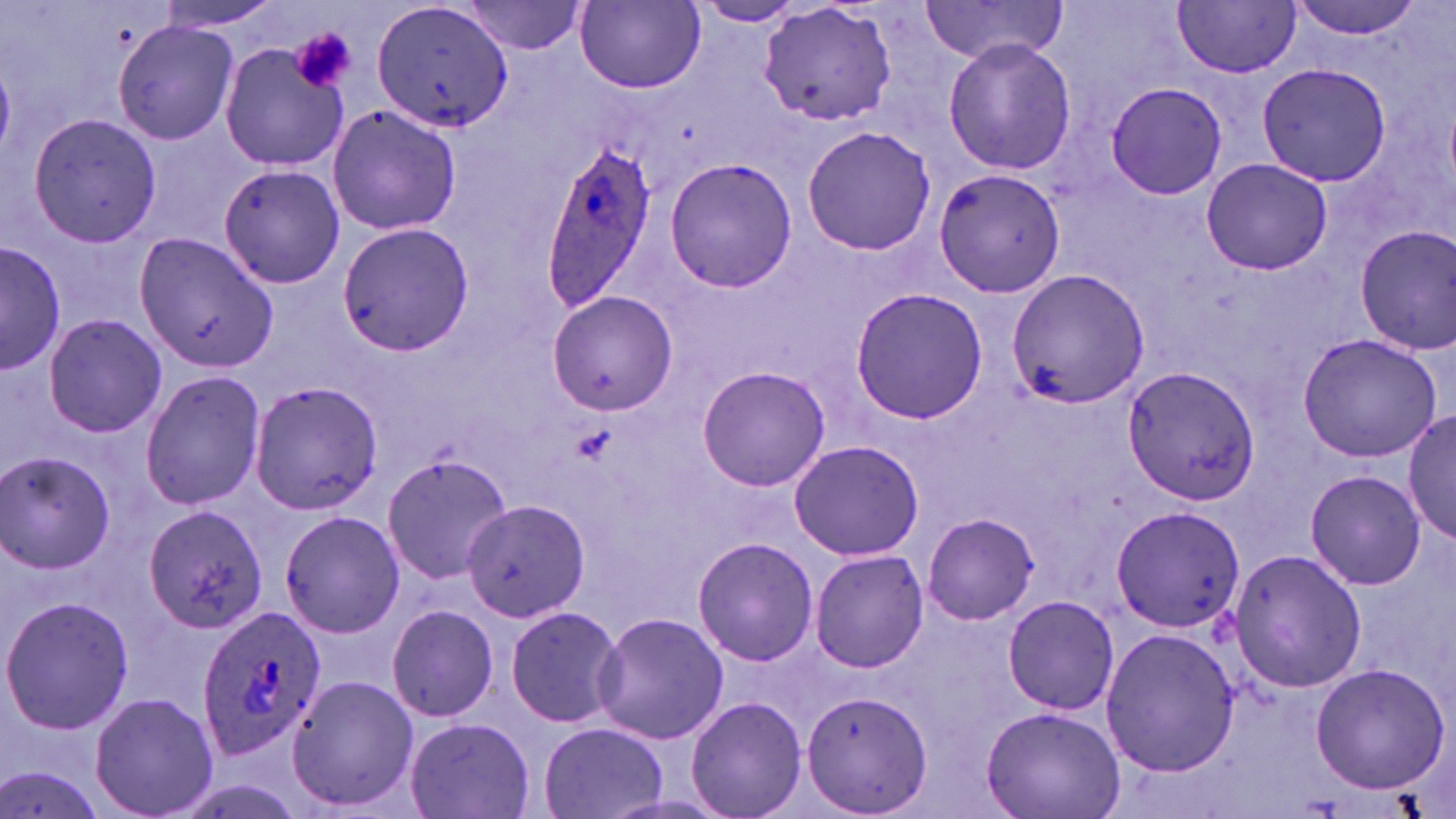 Approximate bounding boxes as [x1, y1, x2, y2] in pixels. Plasmodium ovale-infected red blood cell locations: [540, 136, 663, 312], [196, 605, 328, 761]. Uninfected red blood cell locations: [1288, 0, 1426, 39], [154, 1, 284, 32], [371, 1, 512, 135], [575, 1, 706, 91], [919, 1, 1070, 64], [457, 2, 590, 54], [693, 2, 805, 26], [1174, 2, 1301, 77], [757, 3, 898, 126], [112, 20, 239, 146], [942, 37, 1075, 175], [220, 42, 352, 170], [1257, 64, 1390, 185], [1106, 82, 1228, 201], [328, 102, 461, 236], [26, 112, 163, 248], [800, 125, 936, 255], [664, 157, 800, 291], [1202, 157, 1330, 275], [218, 163, 346, 290], [932, 168, 1066, 298], [339, 222, 474, 356], [1353, 225, 1456, 355], [136, 233, 278, 372], [1, 242, 62, 377], [1007, 267, 1149, 409], [849, 288, 989, 424], [545, 290, 677, 413], [41, 313, 167, 440], [1296, 333, 1443, 463], [1122, 364, 1259, 504], [697, 365, 831, 492], [138, 370, 266, 510], [252, 381, 382, 514], [1405, 407, 1456, 548], [788, 438, 923, 561], [382, 450, 513, 584], [1, 452, 118, 574], [1303, 469, 1428, 590], [464, 499, 588, 623], [1109, 503, 1247, 632], [142, 504, 268, 636], [280, 510, 405, 638], [922, 512, 1040, 624], [694, 535, 817, 667], [1226, 547, 1366, 696], [810, 549, 929, 671], [1, 596, 133, 736], [1003, 596, 1121, 715], [505, 604, 625, 728], [387, 605, 500, 722], [594, 611, 731, 744], [1101, 627, 1241, 778], [1309, 662, 1450, 795], [287, 673, 419, 815], [800, 690, 932, 817], [89, 692, 220, 819], [685, 696, 807, 819], [979, 704, 1124, 819], [404, 717, 535, 819], [537, 721, 670, 819], [2, 766, 105, 819]. Platelet locations: [291, 27, 356, 93]. Slide-level diagnosis: Plasmodium ovale. Captured at 1000x magnification. One field of a larger specimen. Light microscopy. Thin blood film. May-Grünwald-Giemsa-stained preparation. Image is 1456×819 pixels.